Report the malaria status of this cell.
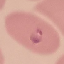

Parasitized.

Automatically extracted cell patch, resized to 64 × 64 pixels. Giemsa-stained preparation. Thin blood film. Acquired by smartphone through the microscope eyepiece.